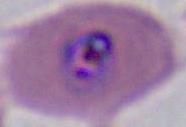
Summary:
  - Modality: micrograph
  - Identification: Plasmodium
  - Magnification: 400x or 1000x